Assess this cell for malaria.
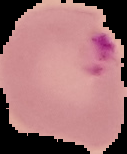
Parasitized.

image type = cell region segmented out of the field of view; surrounding area masked to black
image size = 127×154 pixels
preparation = thin blood smear